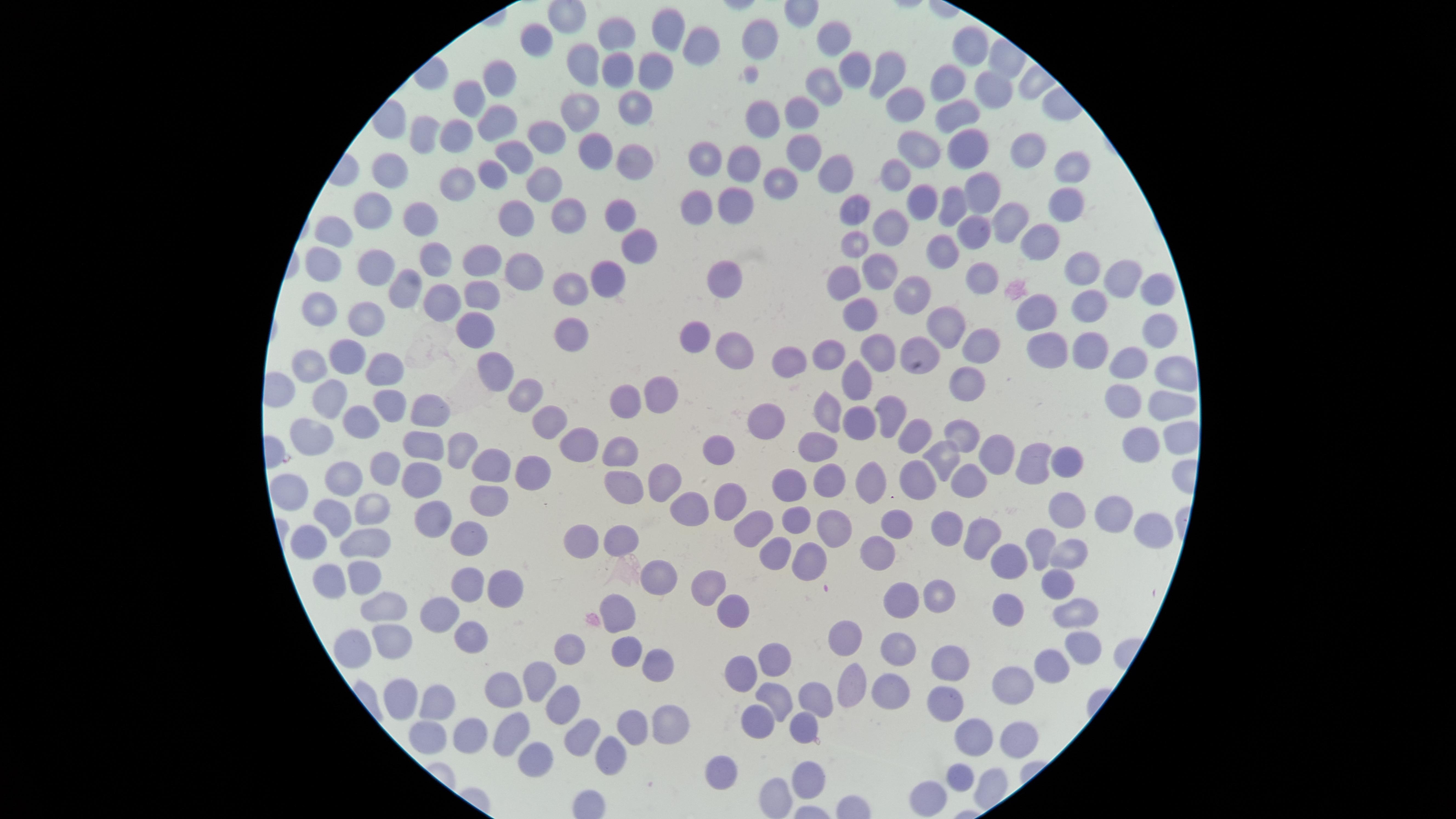

{
  "capture": "smartphone photograph through the microscope eyepiece",
  "preparation": "thin blood smear",
  "uninfected_RBCs": "approximate marker points as [x, y] in pixels: [677, 23], [621, 36], [762, 38], [837, 40], [698, 41], [540, 46], [967, 49], [585, 62], [617, 68], [660, 70], [855, 70], [886, 71], [501, 79], [949, 83], [830, 88], [987, 88], [473, 94], [639, 97], [905, 101], [573, 107], [805, 112], [954, 116], [494, 118], [758, 126], [543, 134], [453, 135], [421, 138], [597, 144], [805, 146], [916, 146], [1026, 147], [963, 150], [515, 154], [707, 154], [746, 158], [629, 160], [1071, 164], [389, 166], [491, 167], [897, 173], [839, 174], [460, 175], [779, 180], [548, 188], [986, 193], [1064, 198], [734, 199], [953, 201], [701, 202], [369, 207], [425, 208], [923, 208], [616, 211], [855, 212], [509, 214], [570, 214], [1013, 217], [897, 226], [338, 227], [972, 232], [853, 240], [1045, 241], [635, 244], [434, 253], [946, 255], [487, 257], [368, 260], [318, 263], [1084, 267], [878, 268], [1117, 271], [977, 272], [728, 273], [611, 274], [523, 277], [570, 280], [845, 280], [409, 281], [1152, 284], [919, 286], [487, 296], [441, 298], [1092, 304], [322, 305], [865, 312], [1046, 313], [363, 318], [952, 319], [473, 324], [1152, 324], [573, 331], [699, 332], [733, 345], [985, 345], [880, 346], [918, 346], [1096, 348], [1056, 349], [348, 351], [830, 353], [787, 360], [308, 366], [1138, 367], [382, 369], [495, 371], [1177, 373], [862, 378], [960, 379], [662, 386], [525, 394], [383, 398], [628, 398], [1120, 399], [329, 400], [1162, 401], [429, 402], [824, 403], [887, 412], [362, 417], [763, 420], [547, 421], [857, 422], [313, 430], [958, 433], [916, 438], [573, 439], [422, 441], [1177, 441], [719, 446], [817, 446], [1138, 448], [467, 449], [988, 452], [620, 454], [941, 456], [1033, 456], [1068, 461], [490, 462], [387, 466], [536, 472], [423, 474], [348, 475], [869, 478], [920, 478], [966, 478], [828, 480], [660, 482], [292, 488], [630, 488], [789, 488], [488, 502], [722, 502], [374, 504], [1066, 510], [689, 512], [1117, 513], [431, 514], [335, 516], [796, 516], [943, 518], [751, 524], [898, 524], [836, 527], [1146, 531], [974, 532], [471, 534], [624, 536], [586, 540], [370, 542], [305, 543], [1042, 544], [1067, 546], [777, 550], [878, 553], [1004, 553], [805, 557], [360, 573], [329, 577], [657, 578], [712, 579], [468, 582], [1056, 586], [503, 588], [902, 593], [939, 595], [736, 604], [1009, 604], [391, 608], [620, 609], [438, 611], [1075, 612], [391, 635], [846, 636], [473, 640], [347, 642], [1082, 644], [897, 645], [564, 646], [621, 647], [776, 656], [654, 661], [950, 661], [1051, 665], [745, 668], [1009, 679], [545, 681], [849, 688], [895, 688], [505, 690], [819, 692], [396, 693], [435, 695], [780, 695], [949, 698], [566, 701], [759, 717], [629, 720], [803, 722], [665, 723], [510, 725], [426, 727], [471, 728], [577, 731], [973, 735], [1012, 736], [615, 747], [528, 751], [723, 768], [803, 773], [960, 778], [935, 790], [769, 795]",
  "stain": "Giemsa",
  "visible_region": "circular",
  "image_size": "1456×819 pixels",
  "field_of_view": "single",
  "presence": "no malaria parasites identified"
}